Assess this cell for malaria.
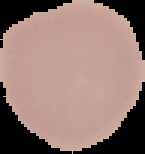

It is uninfected.

The area outside the segmented cell region is set to black. From a thin blood film. Image is 145×154 pixels.